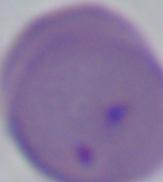

modality = photomicrograph
magnification = 1000x
identification = Babesia